Locate every Plasmodium parasite and every leukocyte.
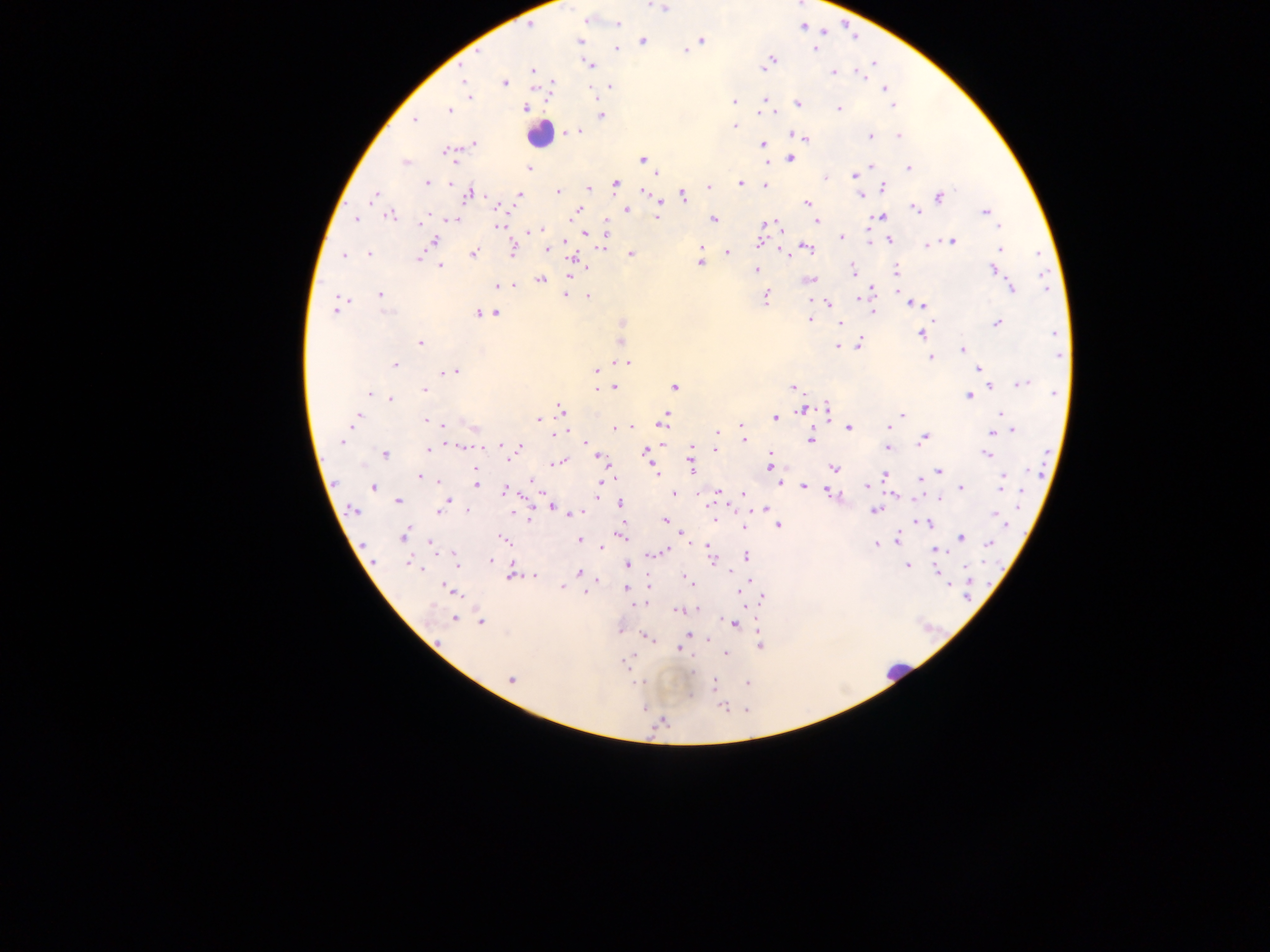
Approximate centers as (x, y) in pixels.
Plasmodium parasites: (663, 7), (587, 21), (617, 24), (580, 40), (702, 40), (643, 41), (616, 49), (815, 49), (684, 50), (771, 59), (590, 65), (765, 68), (533, 69), (834, 71), (861, 75), (504, 82), (465, 83), (552, 84), (610, 86), (885, 89), (469, 97), (765, 99), (890, 99), (733, 101), (798, 103), (892, 106), (526, 109), (838, 109), (766, 110), (450, 111), (601, 116), (414, 119), (734, 126), (571, 132), (576, 133), (796, 135), (871, 135), (899, 136), (804, 138), (473, 145), (763, 145), (447, 153), (642, 159), (791, 159), (405, 162), (870, 165), (908, 167), (529, 168), (855, 174), (826, 177), (427, 183), (450, 183), (617, 183), (740, 183), (765, 185), (589, 187), (708, 187), (884, 187), (557, 191), (644, 191), (468, 194), (519, 194), (374, 195), (860, 195), (683, 196), (939, 197), (806, 203), (659, 205), (501, 208), (626, 209), (915, 209), (577, 211), (985, 211), (390, 216), (657, 216), (880, 217), (356, 220), (453, 220), (713, 220), (817, 221), (421, 222), (770, 223), (499, 225), (777, 226), (998, 227), (540, 230), (605, 233), (586, 234), (842, 237), (434, 240), (889, 240), (565, 241), (952, 241), (758, 242), (603, 244), (928, 244), (700, 247), (1000, 248), (547, 249), (807, 249), (512, 251), (727, 252), (369, 253), (473, 254), (787, 254), (631, 255), (344, 256), (419, 258), (574, 259), (700, 262), (440, 267), (853, 269), (994, 269), (756, 270), (896, 270), (569, 275), (541, 280), (810, 280), (513, 284), (499, 285), (1012, 289), (871, 290), (380, 294), (565, 295), (588, 296), (766, 298), (340, 301), (828, 303), (920, 305), (335, 310), (873, 312), (496, 313), (479, 314), (810, 320), (840, 323), (997, 323), (1056, 333), (921, 334), (420, 343), (859, 343), (838, 347), (962, 349), (1059, 356), (931, 357), (621, 363), (627, 363), (395, 365), (979, 368), (455, 371), (597, 371), (446, 372), (983, 373), (1022, 384), (989, 385), (615, 387), (674, 387), (793, 387), (425, 389), (598, 389), (369, 394), (1055, 394), (968, 396), (390, 398), (561, 408), (828, 408), (803, 411), (1001, 414), (902, 415), (358, 416), (775, 417), (538, 419), (427, 420), (663, 422), (442, 424), (474, 427), (741, 427), (888, 427), (615, 428), (849, 428), (1013, 431), (559, 432), (717, 432), (992, 432), (924, 438), (744, 439), (811, 440), (342, 441), (585, 442), (500, 445), (466, 447), (519, 447), (691, 447), (887, 447), (429, 450), (716, 450), (646, 451), (985, 453), (385, 454), (601, 458), (558, 462), (692, 466), (770, 466), (652, 467), (834, 467), (939, 471), (475, 472), (655, 472), (420, 476), (884, 476), (1003, 478), (920, 479), (531, 481), (440, 482), (601, 482), (476, 483), (780, 483), (866, 485), (1000, 485), (803, 486), (374, 487), (961, 487), (504, 491), (675, 492), (719, 492), (743, 493), (830, 494), (599, 495), (939, 498), (398, 501), (448, 502), (620, 503), (552, 506), (765, 508), (352, 509), (439, 511), (874, 511), (468, 512), (577, 513), (999, 517), (665, 521), (926, 523), (744, 526), (778, 526), (682, 534), (404, 535), (621, 535), (960, 537), (898, 539), (505, 540), (580, 540), (989, 543), (877, 544), (433, 545), (601, 549), (937, 551), (663, 552), (711, 556), (745, 556), (455, 557), (490, 561), (457, 562), (408, 563), (627, 565), (907, 565), (579, 572), (511, 573), (940, 573), (535, 577), (687, 578), (749, 580), (562, 587), (625, 589), (451, 590), (586, 593), (762, 597), (637, 605), (696, 609), (679, 610), (455, 619), (481, 622), (733, 624), (688, 634), (647, 636), (759, 646), (679, 649), (725, 654), (629, 658), (692, 672), (511, 680), (638, 682), (748, 683), (715, 684), (722, 707), (663, 722).
Leukocytes: (540, 135), (895, 671).

country = Ghana
image size = 1270×952 pixels
capture = mobile-phone photograph through a microscope
field of view = single
preparation = thick blood film